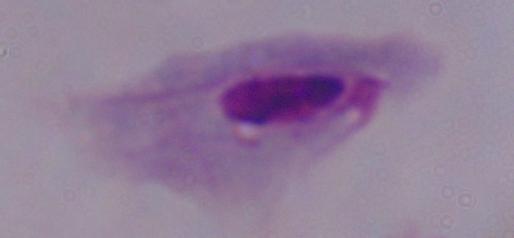

modality = photomicrograph
identification = trichomonad
magnification = 1000x